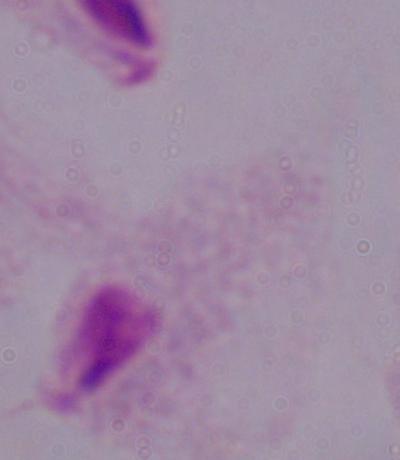

identification = trichomonad
modality = photomicrograph
magnification = 1000x